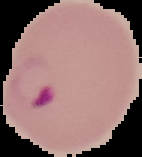

malaria_status: parasitized
image_size: 142×157 pixels
image_type: segmented cell region on a black background
preparation: thin blood smear